Report the malaria status of this cell.
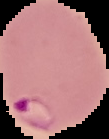
Parasitized.

image size = 109×139 pixels
image type = cell region segmented out of the field of view; surrounding area masked to black
preparation = thin blood smear